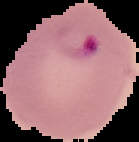

result: malaria parasites identified
image_size: 139×142 pixels
preparation: thin blood smear
image_type: cell region segmented out of the field of view; surrounding area masked to black